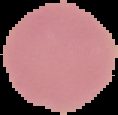

Segmented cell region on a black background. Image is 118×115 pixels. From a thin blood smear. Malaria status: uninfected.